Classify this cell by malaria status.
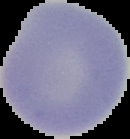

Uninfected.

From a thin blood film. Image is 130×139 pixels. The area outside the segmented cell region is set to black.